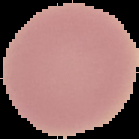

Malaria status: uninfected. From a thin blood film. The area outside the segmented cell region is set to black. Image is 139×139 pixels.